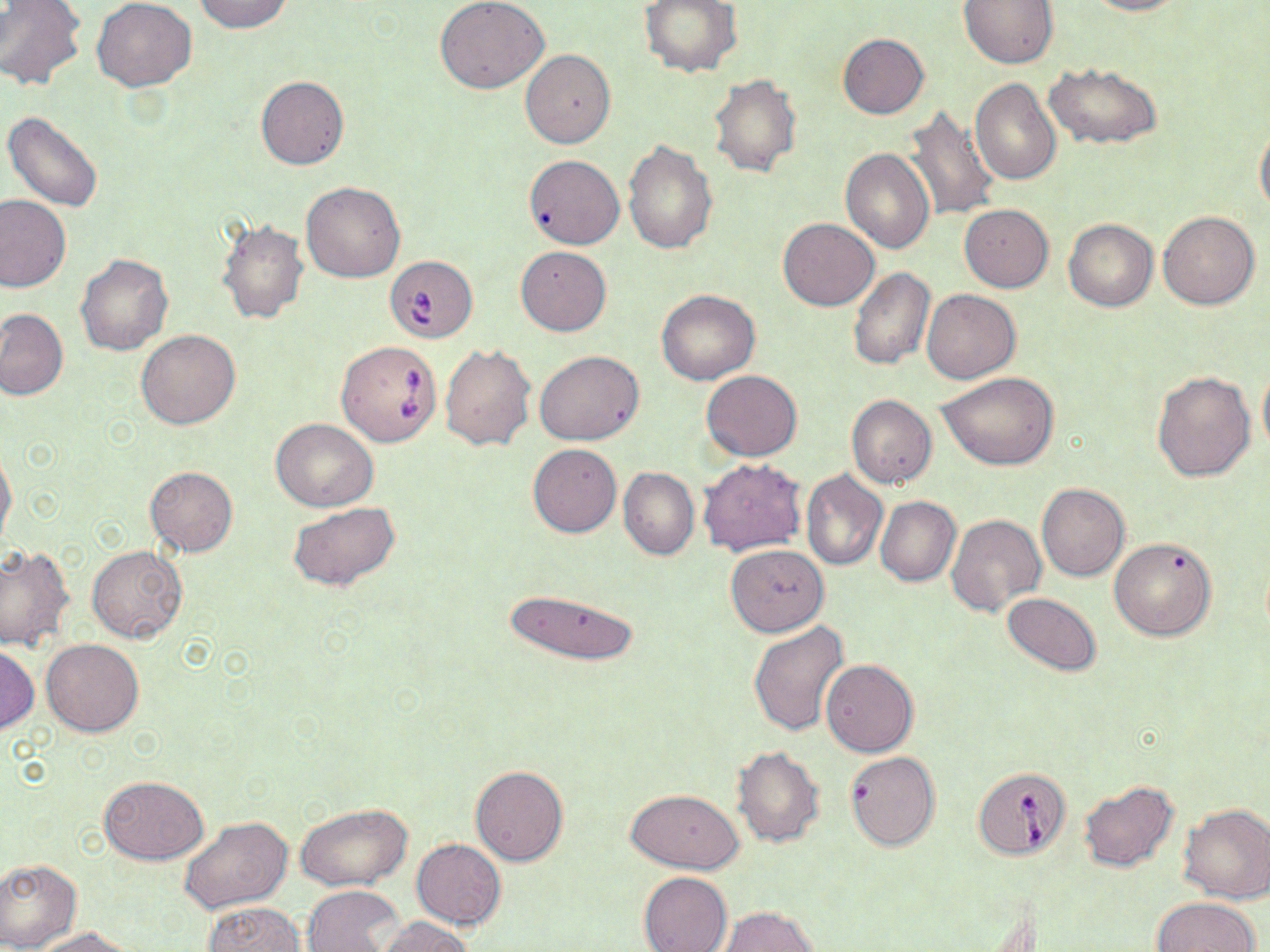
slide-level diagnosis = Babesia divergens
stain = May-Grünwald-Giemsa
preparation = thin blood smear
image size = 1270×952 pixels
modality = light microscopy
Babesia divergens-infected red blood cell locations = approximate bounding boxes as named x1/y1/x2/y2 corners in pixels: (x1=387, y1=257, x2=474, y2=344), (x1=335, y1=340, x2=443, y2=446), (x1=973, y1=767, x2=1070, y2=860)
magnification = 1000x
uninfected red blood cell locations = approximate bounding boxes as named x1/y1/x2/y2 corners in pixels: (x1=92, y1=0, x2=196, y2=91), (x1=191, y1=0, x2=292, y2=33), (x1=436, y1=0, x2=548, y2=94), (x1=640, y1=0, x2=742, y2=77), (x1=959, y1=0, x2=1059, y2=69), (x1=1082, y1=0, x2=1188, y2=16), (x1=0, y1=1, x2=86, y2=90), (x1=837, y1=33, x2=929, y2=119), (x1=520, y1=50, x2=615, y2=148), (x1=1044, y1=62, x2=1161, y2=149), (x1=708, y1=73, x2=801, y2=177), (x1=255, y1=76, x2=350, y2=170), (x1=971, y1=76, x2=1061, y2=184), (x1=900, y1=106, x2=1000, y2=220), (x1=4, y1=111, x2=104, y2=212), (x1=1256, y1=123, x2=1270, y2=218), (x1=624, y1=139, x2=718, y2=254), (x1=841, y1=148, x2=933, y2=253), (x1=523, y1=154, x2=624, y2=249), (x1=301, y1=181, x2=406, y2=283), (x1=0, y1=195, x2=71, y2=292), (x1=959, y1=204, x2=1053, y2=292), (x1=1158, y1=210, x2=1260, y2=309), (x1=778, y1=218, x2=879, y2=311), (x1=1064, y1=219, x2=1157, y2=311), (x1=216, y1=220, x2=309, y2=325), (x1=516, y1=245, x2=612, y2=335), (x1=76, y1=254, x2=173, y2=355), (x1=848, y1=267, x2=935, y2=370), (x1=922, y1=289, x2=1020, y2=384), (x1=657, y1=290, x2=760, y2=384), (x1=0, y1=308, x2=68, y2=400), (x1=136, y1=329, x2=240, y2=429), (x1=439, y1=342, x2=535, y2=451), (x1=535, y1=350, x2=644, y2=446), (x1=1258, y1=365, x2=1270, y2=460), (x1=1151, y1=369, x2=1255, y2=480), (x1=701, y1=370, x2=802, y2=462), (x1=939, y1=372, x2=1059, y2=470), (x1=847, y1=394, x2=937, y2=487), (x1=272, y1=420, x2=378, y2=510), (x1=528, y1=443, x2=621, y2=537), (x1=0, y1=449, x2=17, y2=548), (x1=698, y1=458, x2=807, y2=555), (x1=144, y1=466, x2=238, y2=557), (x1=619, y1=466, x2=699, y2=560), (x1=801, y1=470, x2=888, y2=570), (x1=1037, y1=484, x2=1130, y2=581), (x1=876, y1=496, x2=960, y2=587), (x1=289, y1=501, x2=401, y2=592), (x1=945, y1=515, x2=1046, y2=618), (x1=1109, y1=537, x2=1217, y2=641), (x1=725, y1=544, x2=829, y2=637), (x1=0, y1=545, x2=74, y2=650), (x1=87, y1=545, x2=187, y2=643), (x1=505, y1=587, x2=641, y2=666), (x1=1003, y1=592, x2=1102, y2=676), (x1=750, y1=621, x2=850, y2=736), (x1=41, y1=638, x2=144, y2=735), (x1=1, y1=646, x2=38, y2=732), (x1=821, y1=659, x2=918, y2=757), (x1=732, y1=746, x2=825, y2=847), (x1=845, y1=750, x2=941, y2=852), (x1=471, y1=766, x2=568, y2=866), (x1=99, y1=776, x2=207, y2=864), (x1=1078, y1=780, x2=1179, y2=872), (x1=626, y1=788, x2=744, y2=872), (x1=296, y1=802, x2=414, y2=891), (x1=1178, y1=803, x2=1270, y2=903), (x1=180, y1=816, x2=292, y2=915), (x1=410, y1=838, x2=507, y2=929), (x1=0, y1=857, x2=83, y2=951), (x1=638, y1=872, x2=732, y2=952), (x1=302, y1=885, x2=404, y2=952), (x1=1151, y1=897, x2=1260, y2=952), (x1=200, y1=901, x2=305, y2=952), (x1=719, y1=906, x2=817, y2=952), (x1=378, y1=916, x2=472, y2=952), (x1=33, y1=926, x2=138, y2=951)
field of view = one of a larger specimen